Assess this cell for malaria.
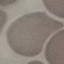
It is uninfected.

image type = cell patch, automatically extracted from a larger field of view and resized to 64 × 64 pixels
stain = Giemsa
capture = smartphone through the microscope eyepiece
preparation = thin blood smear